Outline each blood parasite and name the species.
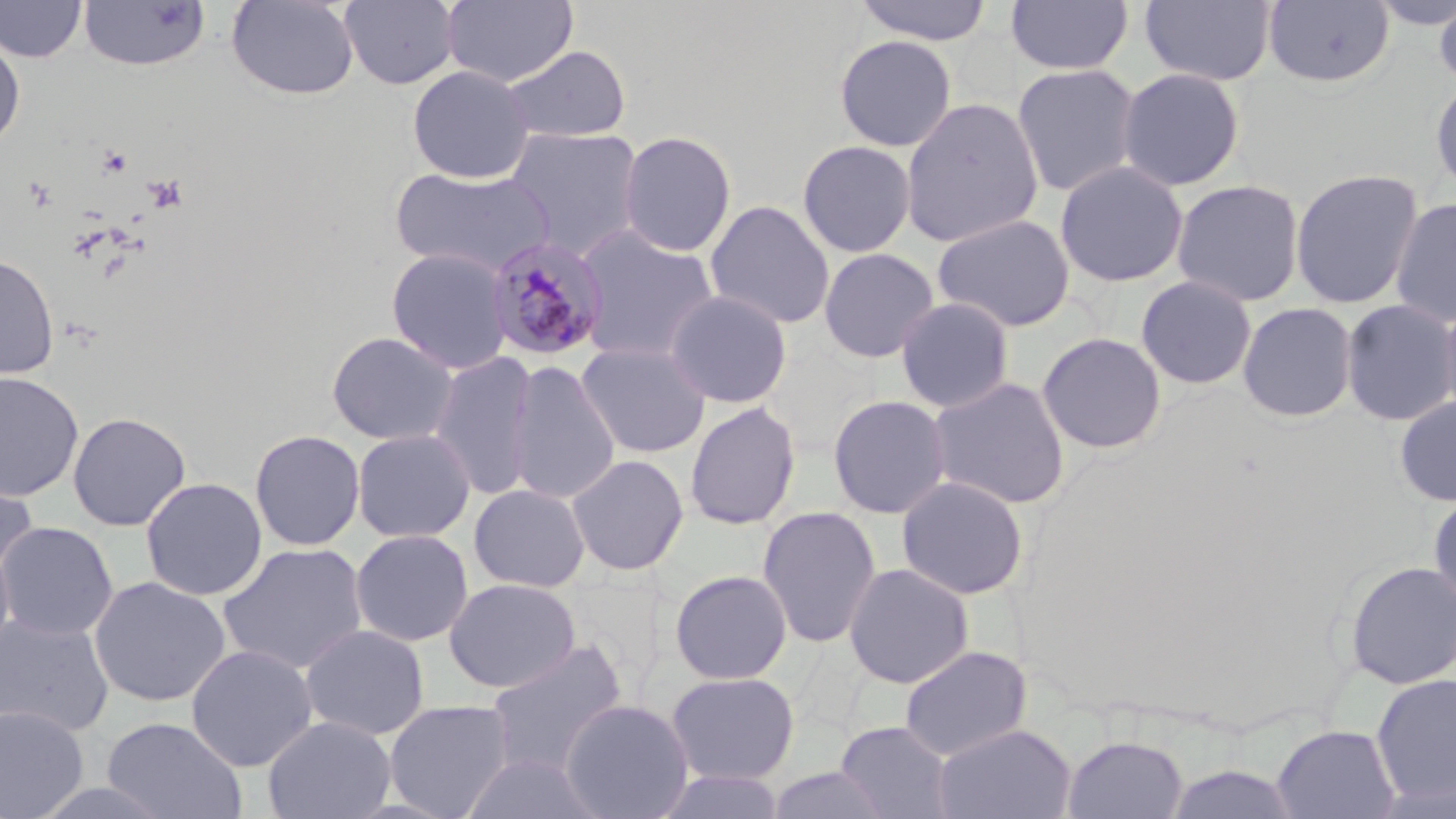

Approximate bounding boxes as (x1,y1)-(x2,y2) corner pairs in pixels.
Plasmodium malariae-infected red blood cells: (484,235)-(611,362).
No Plasmodium falciparum, Plasmodium ovale, Plasmodium vivax, Babesia divergens, or Trypanosoma brucei observed.

slide-level diagnosis = Plasmodium malariae
stain = May-Grünwald-Giemsa
modality = light microscopy
preparation = thin blood smear
platelet locations = approximate bounding boxes as (x1,y1)-(x2,y2) corner pairs in pixels: (96,145)-(133,179), (146,174)-(188,213)
image size = 1456×819 pixels
uninfected red blood cell locations = approximate bounding boxes as (x1,y1)-(x2,y2) corner pairs in pixels: (226,0)-(359,100), (339,0)-(460,89), (442,0)-(579,88), (852,0)-(994,46), (1005,0)-(1134,76), (1139,0)-(1277,86), (1263,0)-(1395,88), (1366,0)-(1455,30), (1434,0)-(1456,94), (0,1)-(87,63), (78,1)-(210,72), (0,34)-(26,150), (834,34)-(957,152), (501,45)-(631,143), (1011,63)-(1143,198), (407,64)-(534,184), (1116,67)-(1246,191), (1430,76)-(1456,196), (901,97)-(1044,247), (505,126)-(646,261), (617,130)-(737,257), (796,139)-(917,257), (1054,160)-(1189,288), (390,165)-(557,277), (1289,168)-(1424,310), (1170,179)-(1305,307), (1390,195)-(1456,329), (704,200)-(835,329), (932,213)-(1076,332), (570,224)-(720,365), (386,247)-(513,375), (818,247)-(939,363), (0,253)-(59,380), (1135,275)-(1258,390), (664,289)-(793,409), (894,295)-(1016,413), (1439,296)-(1456,425), (1340,299)-(1456,427), (1237,302)-(1358,422), (326,331)-(459,446), (1036,332)-(1167,454), (575,341)-(712,458), (428,351)-(539,500), (506,359)-(620,505), (0,371)-(84,501), (927,376)-(1071,510), (827,394)-(952,519), (1395,395)-(1456,507), (683,401)-(801,530), (67,411)-(191,531), (351,427)-(477,543), (249,429)-(366,551), (566,454)-(689,575), (0,469)-(38,589), (896,475)-(1029,600), (140,477)-(267,601), (469,484)-(590,592), (1428,489)-(1456,608), (757,506)-(882,648), (0,521)-(119,641), (350,529)-(474,646), (0,534)-(16,666), (217,542)-(370,675), (1344,559)-(1456,690), (843,562)-(975,689), (669,569)-(793,685), (89,576)-(231,708), (443,578)-(580,693), (1,611)-(115,738), (300,624)-(430,741), (484,638)-(628,778), (185,644)-(318,772), (899,645)-(1034,761), (665,671)-(800,786), (1370,673)-(1456,806), (560,698)-(695,819), (384,699)-(515,818), (0,704)-(89,818), (262,715)-(396,819), (101,716)-(248,819), (835,720)-(956,819), (932,721)-(1075,819), (1271,724)-(1401,819), (1062,734)-(1189,818), (460,752)-(606,819), (1161,763)-(1304,819), (764,767)-(893,819), (652,768)-(787,818)
magnification = 1000x
field of view = single